Identify the blood parasite species.
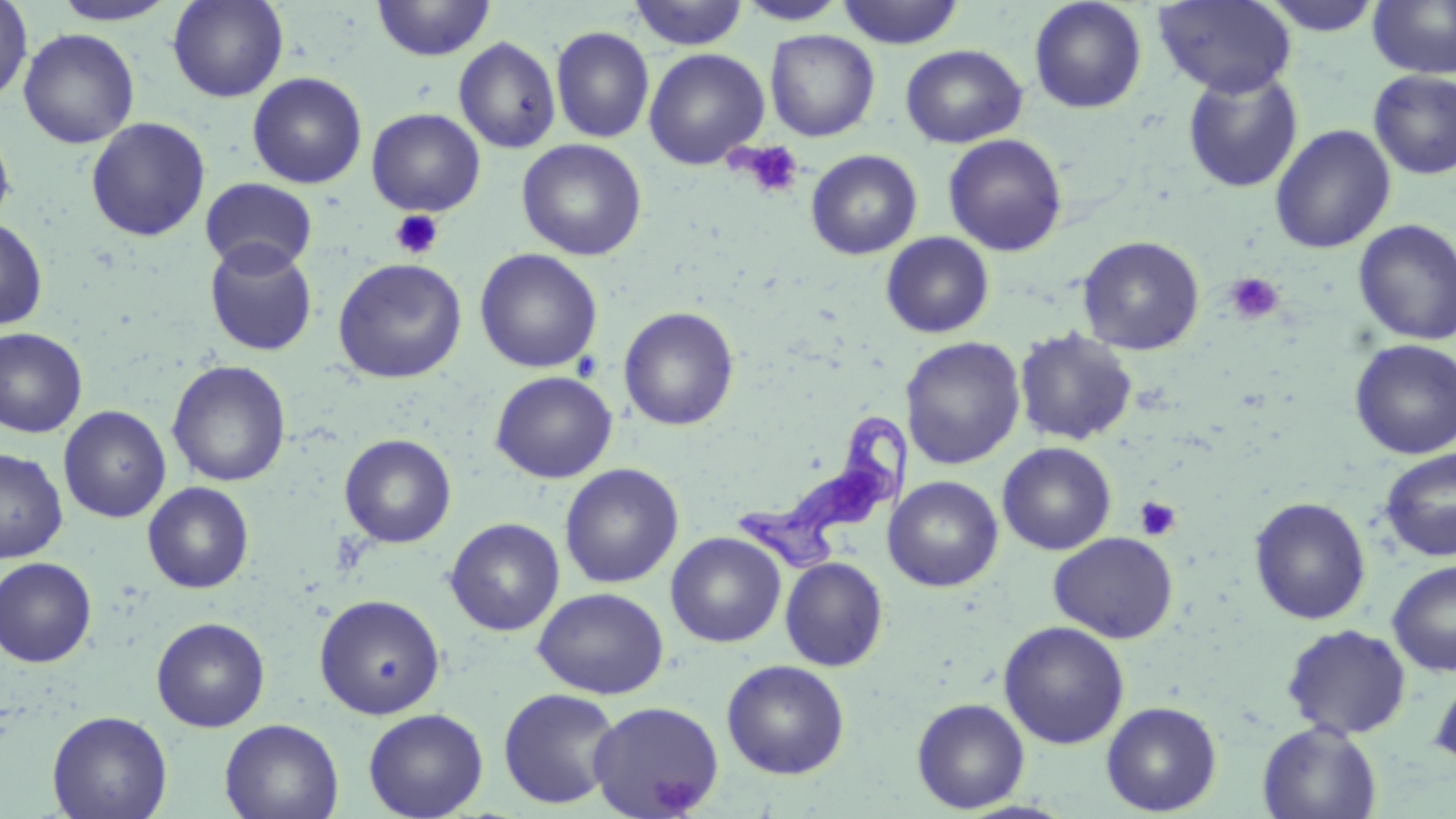
Trypanosoma brucei.

Summary:
  - Coordinate format: approximate bounding boxes as (x1,y1)-(x2,y2) corner pairs in pixels
  - Trypanosoma brucei locations: (736,406)-(916,579)
  - Uninfected red blood cell locations: (0,0)-(33,105), (167,0)-(289,103), (628,0)-(749,50), (1154,0)-(1296,98), (1257,0)-(1386,36), (1367,0)-(1456,79), (50,1)-(179,26), (372,1)-(496,61), (736,1)-(850,26), (836,1)-(966,49), (1029,1)-(1147,114), (551,26)-(654,144), (18,28)-(140,149), (765,29)-(880,142), (453,36)-(561,154), (900,44)-(1027,148), (643,48)-(769,169), (1182,68)-(1303,193), (1369,69)-(1456,179), (247,72)-(367,189), (366,107)-(486,216), (85,116)-(211,241), (0,122)-(16,229), (1270,124)-(1396,254), (943,133)-(1068,257), (517,139)-(647,261), (805,149)-(923,260), (200,178)-(318,274), (0,216)-(48,330), (1353,219)-(1456,345), (881,232)-(995,339), (1077,235)-(1205,355), (203,240)-(318,356), (474,248)-(602,373), (332,258)-(467,382), (619,306)-(739,431), (1014,327)-(1138,446), (0,328)-(87,438), (900,337)-(1026,469), (1350,339)-(1456,459), (167,360)-(292,487), (490,370)-(617,483), (59,405)-(171,523), (339,434)-(456,548), (997,442)-(1117,555), (0,448)-(68,563), (1380,448)-(1456,561), (559,463)-(684,589), (883,476)-(1003,592), (142,481)-(254,593), (1249,496)-(1371,625), (445,517)-(565,636), (1048,531)-(1178,643), (666,532)-(786,648), (0,556)-(98,668), (780,557)-(888,671), (1386,559)-(1456,676), (532,586)-(669,699), (314,594)-(446,719), (151,617)-(270,731), (998,620)-(1130,748), (1282,623)-(1413,740), (722,659)-(849,779), (1428,669)-(1456,772), (498,687)-(622,809), (912,697)-(1030,813), (588,700)-(725,818), (1101,700)-(1222,816), (363,707)-(489,818), (47,710)-(173,819), (219,718)-(344,819), (1257,721)-(1382,819)
  - Platelet locations: (736,141)-(805,199), (390,210)-(444,260), (1224,272)-(1285,325), (1133,496)-(1182,541)
  - Stain: May-Grünwald-Giemsa
  - Preparation: thin blood film
  - Image size: 1456×819 pixels
  - Field of view: one of a larger specimen
  - Magnification: 1000x
  - Modality: optical microscopy